Name the parasite shown.
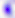
This is Toxoplasma gondii.

Captured at 400x magnification. Micrograph.